Assess this cell for malaria.
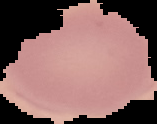
Uninfected.

Summary:
  - Image type: segmented cell region on a black background
  - Preparation: thin blood smear
  - Image size: 157×124 pixels